Report the malaria status of this cell.
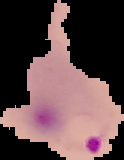

It is parasitized.

Summary:
  - Image type: segmented cell region with the area outside set to black
  - Preparation: thin blood film
  - Image size: 124×160 pixels